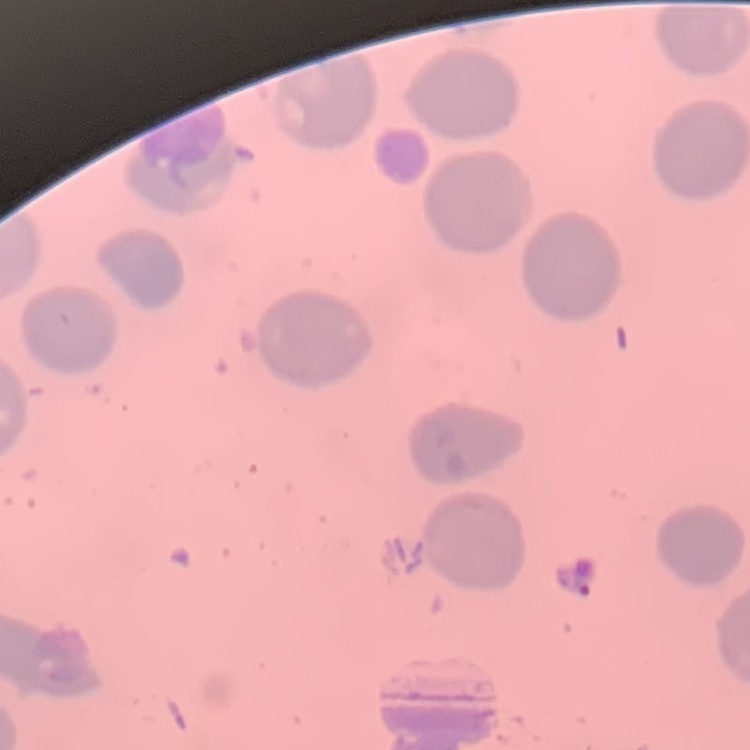
{
  "erythrocyte_morphology": "no rouleaux formation",
  "preparation": "thin blood smear",
  "image_type": "square crop of a larger photomicrograph",
  "stain": "Field's or Giemsa"
}